Describe the morphology of the erythrocytes.
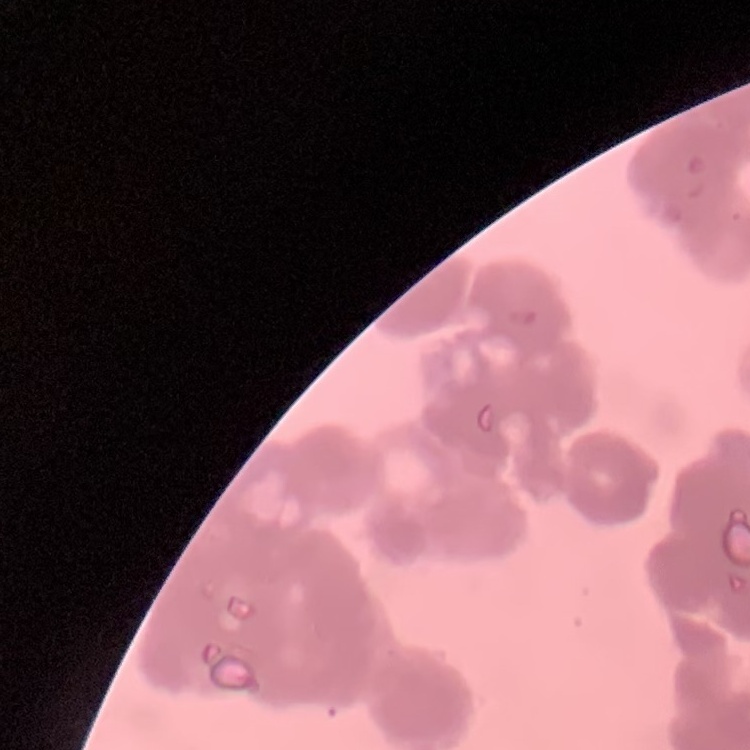
They show rouleaux formation.

Stained with either Field's or Giemsa. Square crop of a larger photomicrograph. Thin blood smear.